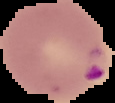

{
  "image_size": "115×103 pixels",
  "image_type": "cell region segmented out of the field of view; surrounding area masked to black",
  "preparation": "thin blood film",
  "malaria_status": "parasitized"
}